Locate every blood parasite and identify its species.
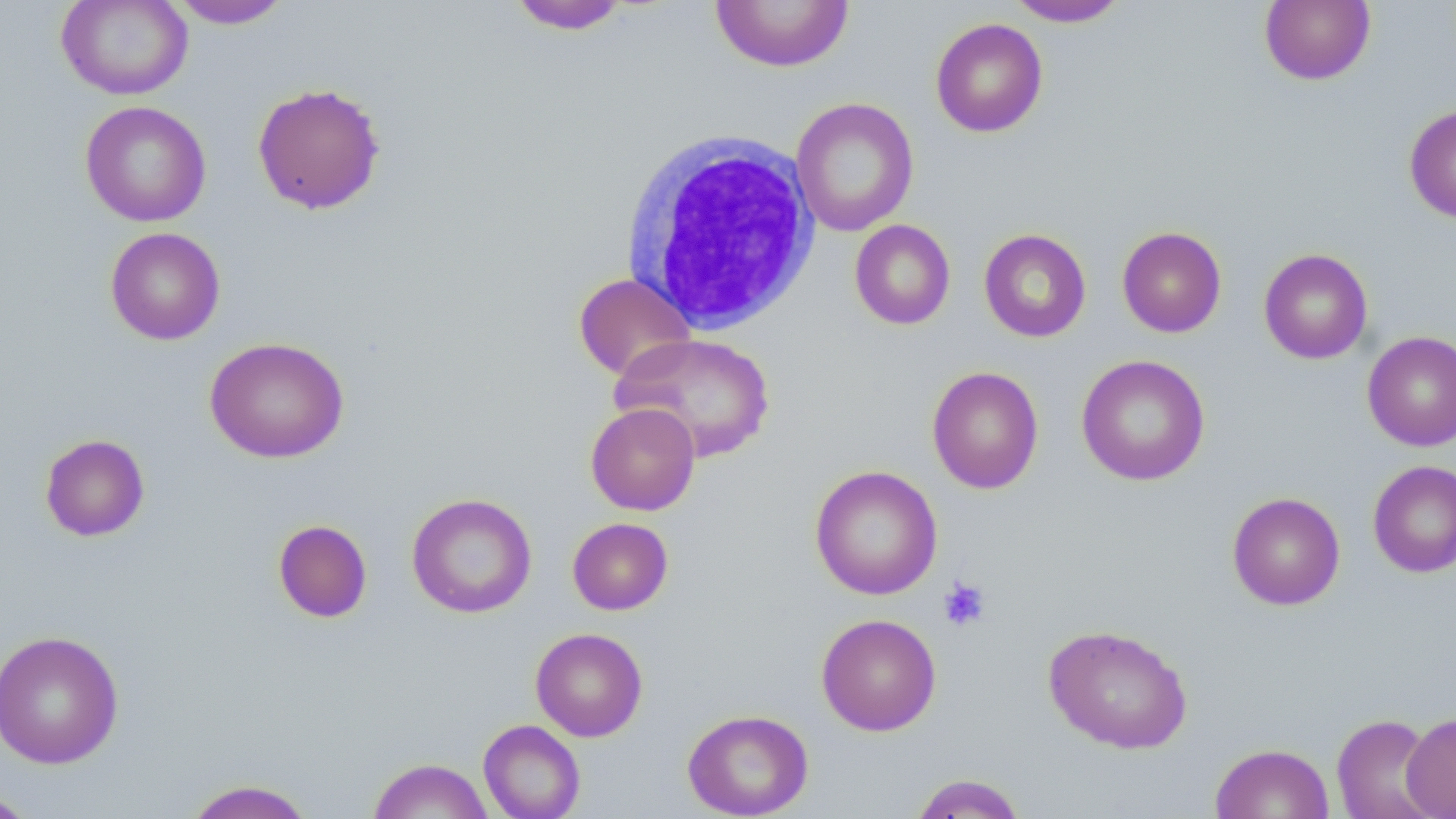

No blood parasites observed.

Summary:
  - Coordinate format: approximate bounding boxes as (x1,y1)-(x2,y2) corner pairs in pixels
  - Uninfected red blood cell locations: (56,0)-(193,100), (710,0)-(855,72), (1006,0)-(1130,27), (168,1)-(294,29), (507,1)-(631,35), (1259,1)-(1376,86), (931,17)-(1048,137), (251,82)-(386,215), (790,97)-(919,236), (79,100)-(211,227), (1404,103)-(1456,224), (850,220)-(956,330), (1116,226)-(1227,337), (105,227)-(225,345), (979,228)-(1091,343), (1259,248)-(1373,364), (573,272)-(697,381), (1362,331)-(1456,452), (612,332)-(777,463), (204,336)-(349,463), (1076,354)-(1211,486), (927,365)-(1044,494), (585,402)-(700,515), (39,433)-(150,542), (1368,460)-(1456,578), (809,465)-(943,600), (1227,491)-(1345,610), (406,492)-(537,618), (567,517)-(673,614), (273,519)-(373,623), (816,613)-(942,736), (1043,624)-(1194,754), (530,627)-(648,741), (0,629)-(124,769), (682,708)-(814,818), (1400,712)-(1456,818), (1332,713)-(1443,819), (478,719)-(586,819), (1210,743)-(1334,819), (367,758)-(494,819), (909,773)-(1028,818), (181,779)-(318,819), (0,788)-(42,818)
  - Platelet locations: (937,577)-(992,632)
  - White blood cell locations: (618,131)-(823,335)
  - Slide-level diagnosis: no evidence of blood parasites
  - Magnification: 1000x
  - Modality: light microscopy
  - Image size: 1456×819 pixels
  - Stain: May-Grünwald-Giemsa
  - Field of view: single
  - Preparation: thin blood film